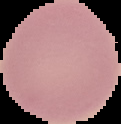

Summary:
  - Preparation: thin blood smear
  - Malaria status: uninfected
  - Image type: segmented cell region on a black background
  - Image size: 121×124 pixels